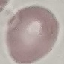

Result: no malaria parasites seen. Thin blood smear. Giemsa-stained preparation. Automatically extracted cell patch, resized to 64 × 64 pixels. Photographed with a smartphone camera at the microscope eyepiece.